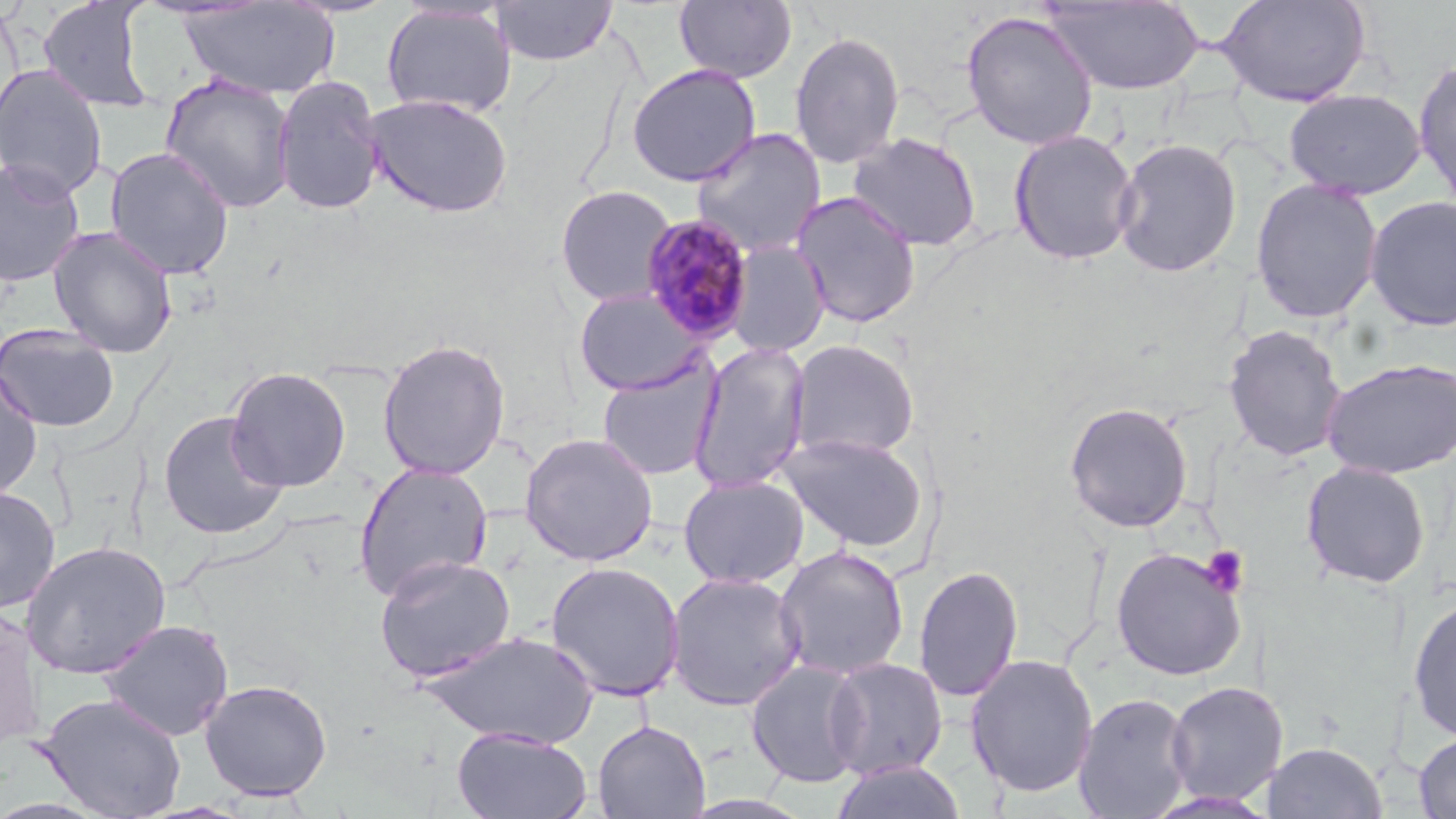 Approximate bounding boxes as (x1, y1, x2, y2) in pixels. Uninfected red blood cell locations: (38, 0, 158, 114), (490, 0, 619, 66), (673, 0, 797, 84), (1042, 1, 1204, 95), (1214, 1, 1372, 107), (177, 2, 341, 100), (380, 3, 517, 119), (960, 10, 1099, 150), (788, 30, 905, 170), (1413, 56, 1456, 206), (0, 63, 108, 200), (625, 63, 762, 187), (160, 73, 297, 214), (272, 73, 386, 216), (639, 84, 802, 242), (1284, 88, 1427, 199), (364, 93, 514, 218), (690, 127, 827, 258), (1008, 129, 1140, 265), (847, 132, 982, 251), (1112, 137, 1242, 277), (104, 146, 235, 280), (0, 157, 86, 288), (1249, 177, 1384, 323), (555, 184, 678, 307), (789, 191, 923, 328), (1364, 195, 1456, 330), (47, 226, 178, 358), (724, 241, 830, 358), (572, 288, 709, 396), (0, 323, 121, 433), (1222, 324, 1348, 462), (377, 338, 511, 480), (788, 339, 920, 462), (687, 340, 812, 495), (597, 356, 723, 481), (1321, 358, 1456, 479), (0, 364, 44, 500), (224, 366, 352, 492), (1064, 401, 1194, 532), (157, 411, 290, 539), (518, 432, 658, 567), (778, 432, 929, 553), (1301, 460, 1431, 589), (352, 461, 493, 602), (678, 474, 809, 589), (0, 485, 61, 614), (20, 539, 172, 679), (773, 545, 910, 681), (1110, 546, 1247, 681), (373, 554, 517, 683), (545, 561, 685, 702), (914, 565, 1023, 703), (665, 572, 806, 711), (1408, 593, 1456, 743), (0, 605, 47, 752), (98, 618, 234, 741), (418, 630, 602, 749), (965, 653, 1099, 798), (824, 657, 948, 780), (746, 659, 868, 788), (199, 679, 333, 801), (1164, 680, 1287, 805), (36, 692, 186, 818), (1074, 692, 1195, 818), (592, 719, 710, 818), (452, 728, 592, 819), (1414, 731, 1456, 818), (1262, 741, 1387, 819), (829, 760, 968, 818). Plasmodium malariae-infected red blood cell locations: (640, 214, 757, 343). Platelet locations: (1200, 545, 1249, 597). Slide-level diagnosis: Plasmodium malariae. May-Grünwald-Giemsa-stained preparation. Light microscopy. 1000x magnification. Thin blood smear. Image is 1456×819 pixels. Single field of view.